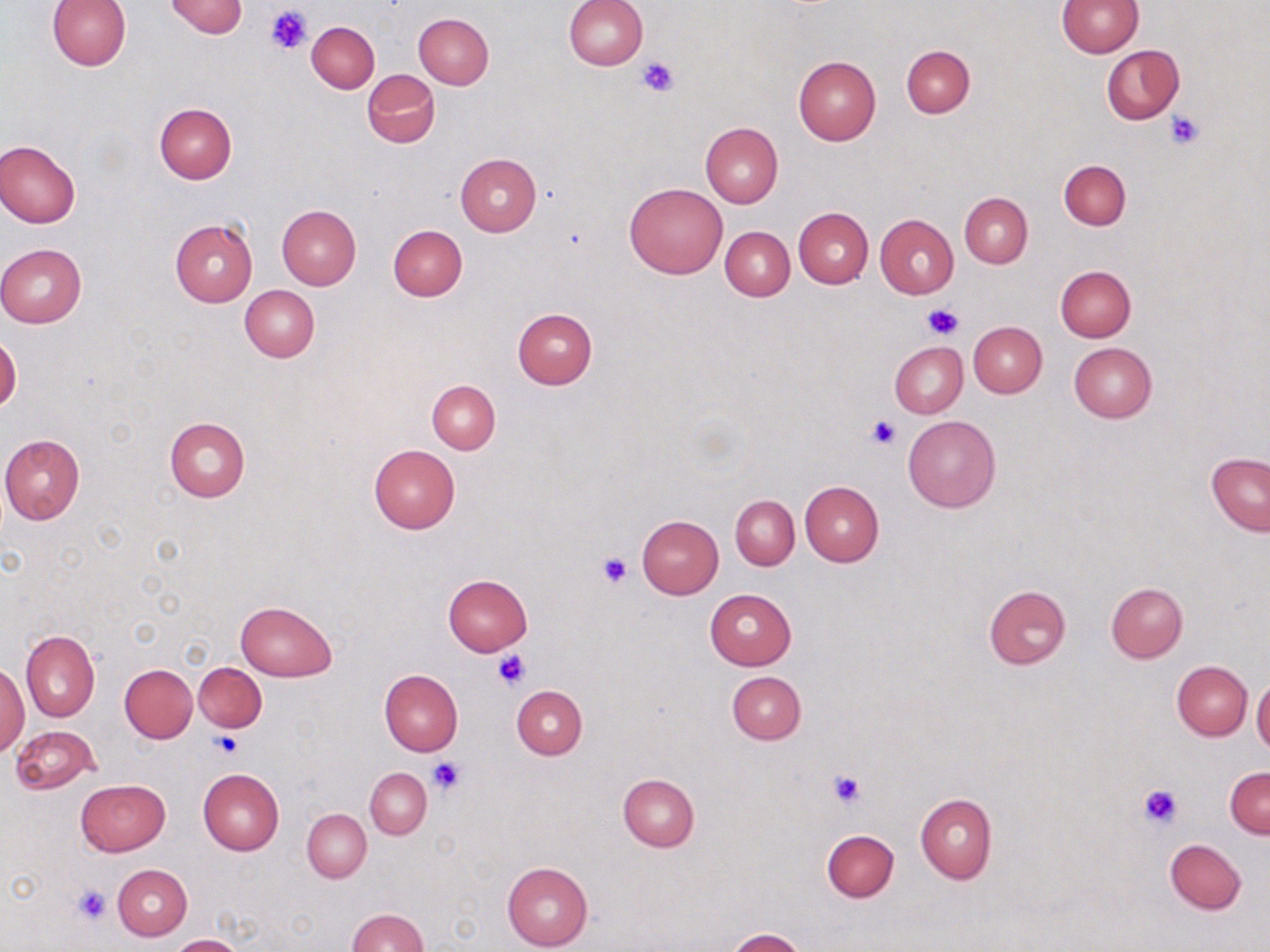

Summary:
  - Coordinate format: approximate bounding boxes as (x1, y1, x2, y2) in pixels
  - Uninfected red blood cell locations: (46, 0, 131, 71), (165, 0, 246, 39), (565, 0, 648, 71), (1055, 0, 1143, 57), (414, 13, 494, 89), (306, 21, 380, 93), (901, 45, 975, 118), (1101, 45, 1185, 124), (794, 56, 881, 145), (362, 69, 440, 148), (154, 103, 236, 184), (701, 122, 782, 208), (1, 140, 81, 228), (456, 153, 541, 235), (1059, 160, 1130, 230), (624, 181, 728, 279), (959, 193, 1032, 268), (277, 206, 362, 289), (793, 207, 873, 288), (875, 214, 959, 299), (169, 217, 259, 307), (388, 225, 467, 301), (721, 226, 795, 300), (0, 244, 87, 327), (1055, 266, 1136, 342), (240, 285, 320, 362), (513, 308, 598, 389), (968, 321, 1047, 398), (0, 336, 21, 412), (890, 341, 967, 418), (1069, 342, 1156, 424), (427, 380, 501, 454), (903, 415, 1000, 512), (164, 417, 251, 502), (0, 434, 86, 525), (369, 444, 460, 532), (1206, 453, 1270, 535), (799, 480, 884, 566), (730, 495, 800, 569), (637, 515, 724, 598), (443, 574, 532, 655), (1105, 583, 1187, 663), (983, 585, 1071, 670), (705, 589, 797, 669), (235, 601, 338, 681), (19, 629, 99, 722), (1172, 660, 1252, 740), (0, 662, 29, 756), (194, 663, 265, 732), (119, 664, 197, 743), (379, 669, 463, 757), (726, 671, 806, 745), (1251, 678, 1270, 755), (512, 685, 588, 759), (10, 725, 99, 794), (1225, 766, 1269, 839), (365, 768, 431, 839), (198, 769, 283, 856), (618, 774, 699, 852), (75, 779, 170, 856), (915, 792, 997, 883), (303, 809, 371, 881), (822, 829, 899, 902), (1164, 839, 1246, 914), (501, 860, 592, 951), (113, 865, 191, 940), (346, 909, 427, 952), (725, 928, 805, 952), (171, 934, 245, 952)
  - Platelet locations: (267, 3, 311, 55), (638, 55, 679, 97), (1167, 111, 1204, 147), (922, 302, 964, 340), (867, 415, 902, 450), (598, 552, 632, 587), (492, 648, 530, 691), (212, 730, 242, 758), (427, 756, 464, 794), (829, 770, 865, 807), (1138, 782, 1184, 829), (72, 884, 112, 925)
  - Slide-level diagnosis: no evidence of blood parasites
  - Magnification: 1000x
  - Image size: 1270×952 pixels
  - Stain: May-Grünwald-Giemsa
  - Preparation: thin blood film
  - Field of view: one of a larger specimen
  - Modality: optical microscopy